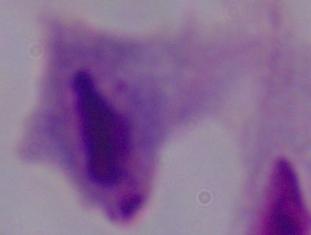 1000x magnification. A trichomonad is seen. Photomicrograph.